Outline each uninfected red blood cell.
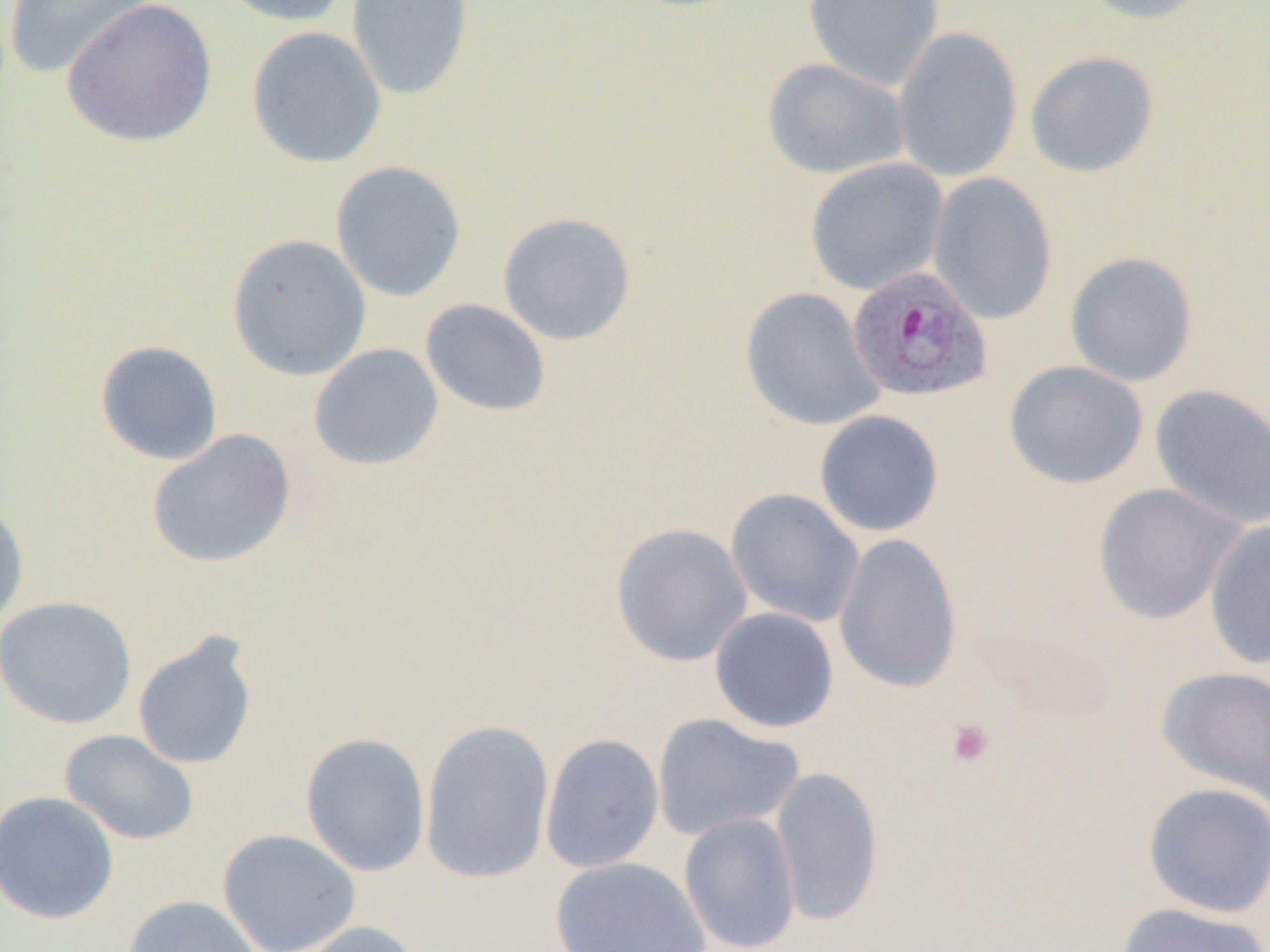
Approximate bounding boxes as (x1, y1, x2, y2) in pixels.
Uninfected red blood cells: (3, 0, 158, 79), (61, 0, 218, 148), (212, 0, 351, 27), (347, 0, 475, 102), (803, 0, 944, 91), (1073, 0, 1212, 25), (246, 26, 387, 168), (892, 26, 1024, 184), (1025, 50, 1158, 178), (762, 57, 909, 181), (805, 158, 948, 295), (330, 160, 467, 302), (927, 172, 1058, 325), (497, 211, 637, 346), (227, 233, 372, 380), (1065, 251, 1198, 387), (740, 286, 885, 431), (420, 299, 551, 417), (94, 340, 223, 465), (309, 343, 444, 470), (1004, 360, 1148, 489), (1150, 384, 1270, 530), (814, 410, 944, 537), (147, 429, 296, 569), (1093, 482, 1246, 624), (726, 488, 865, 629), (0, 500, 29, 631), (1204, 520, 1270, 669), (611, 523, 753, 666), (833, 532, 962, 695), (0, 595, 137, 729), (709, 608, 839, 733), (132, 631, 259, 771), (1156, 666, 1269, 806), (652, 713, 804, 842), (419, 718, 555, 884), (60, 729, 200, 845), (300, 732, 431, 877), (540, 733, 664, 873), (770, 766, 884, 927), (1142, 782, 1270, 918), (0, 790, 120, 925), (679, 813, 801, 952), (217, 828, 361, 952), (551, 857, 711, 952), (122, 894, 263, 952), (1116, 901, 1268, 952), (291, 920, 426, 952).

Summary:
  - Plasmodium ovale-infected red blood cell locations: (846, 265, 993, 404)
  - Platelet locations: (946, 719, 994, 768)
  - Slide-level diagnosis: Plasmodium ovale
  - Preparation: thin blood smear
  - Field of view: one of a larger specimen
  - Modality: light microscopy
  - Image size: 1270×952 pixels
  - Magnification: 1000x